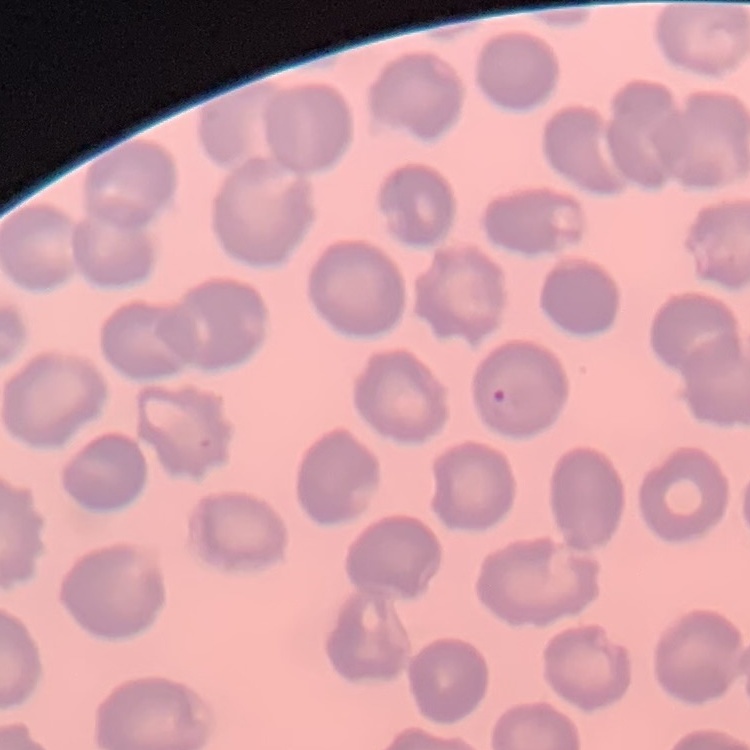
red_blood_cell_morphology: no rouleaux formation
image_type: one tile cut from a larger photomicrograph
preparation: thin blood film
stain: Field's or Giemsa